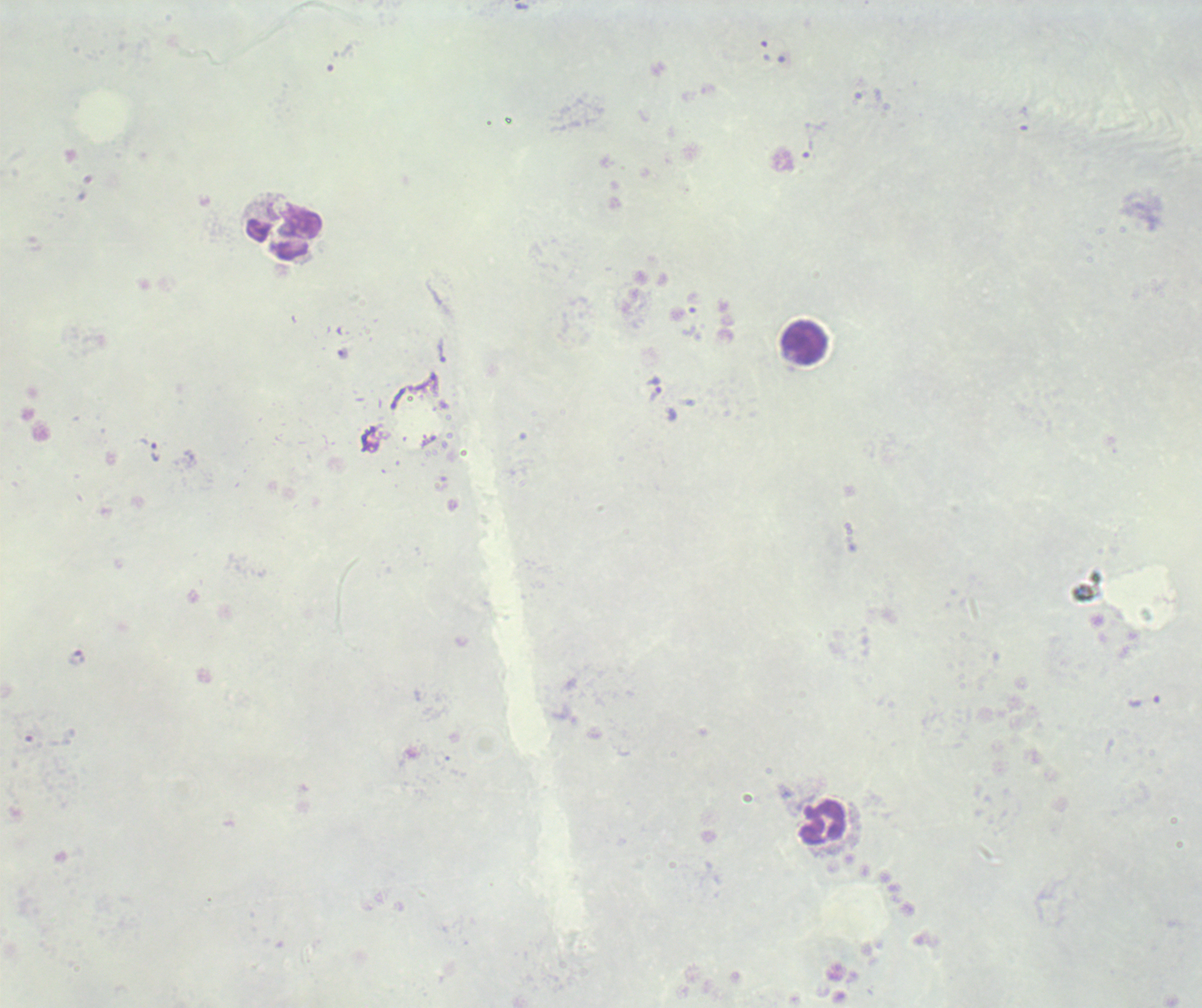

Approximate centers as {x, y} in pixels.
Summary:
  - Trophozoite locations: {442, 351}, {655, 391}, {150, 449}, {77, 658}, {1144, 702}
  - Leukocyte locations: {284, 233}, {804, 344}, {824, 823}
  - Result: malaria parasites identified
  - Field of view: one from this slide
  - Magnification: 100x
  - Background quality: unsatisfactory
  - Context: previously used in an actual diagnosis
  - Image size: 1202×1008 pixels
  - Preparation: thick blood smear
  - Stain: Romanowsky
  - Coloration quality: bad